Identify the preparation type.
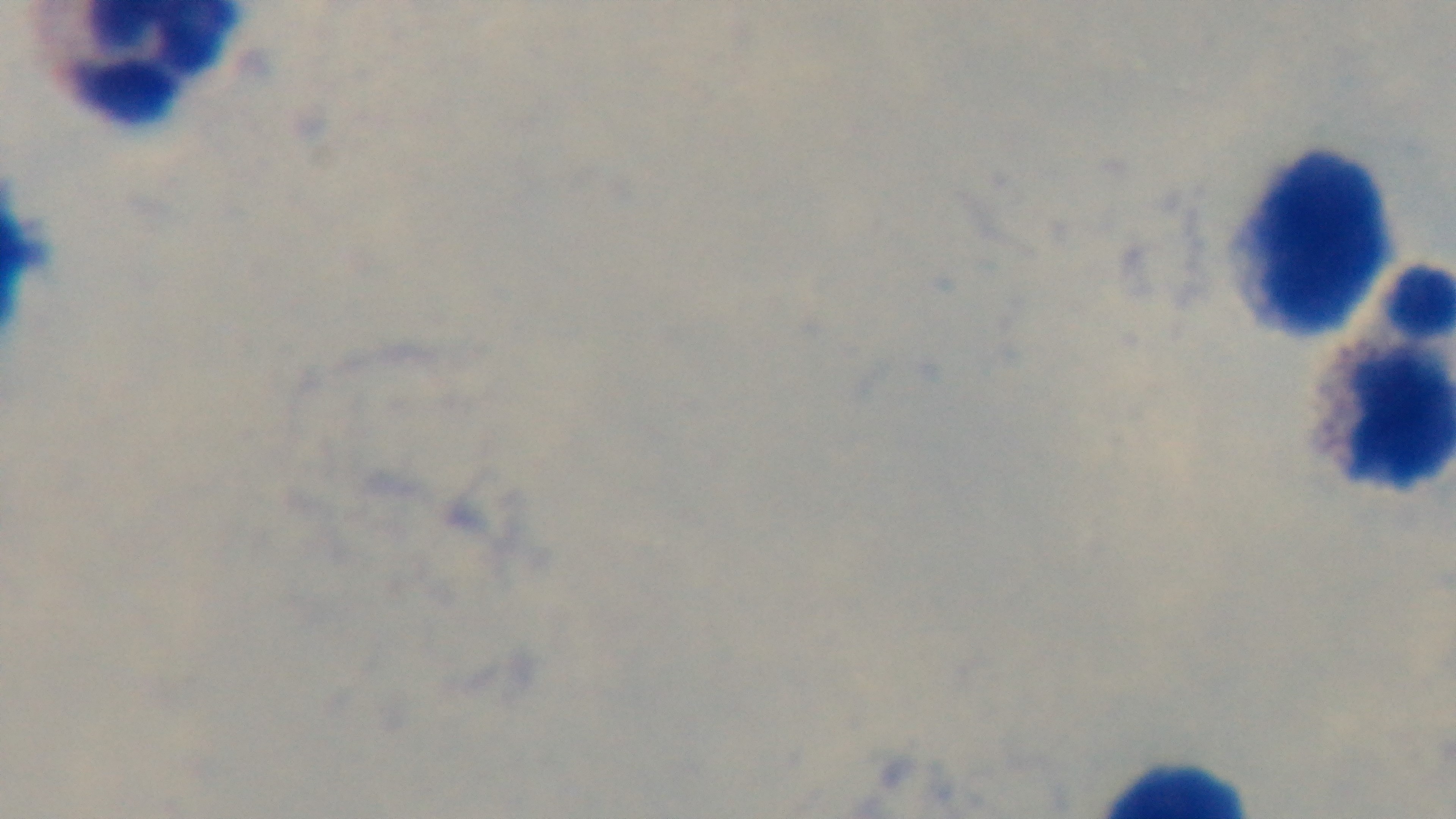

Thick.

Summary:
  - Stain: Giemsa
  - Objective: 100x oil immersion
  - Capture: mounted 4K digital camera
  - Modality: light microscopy
  - Malaria status: uninfected
  - Field of view: one from the slide